Point out each Plasmodium parasite.
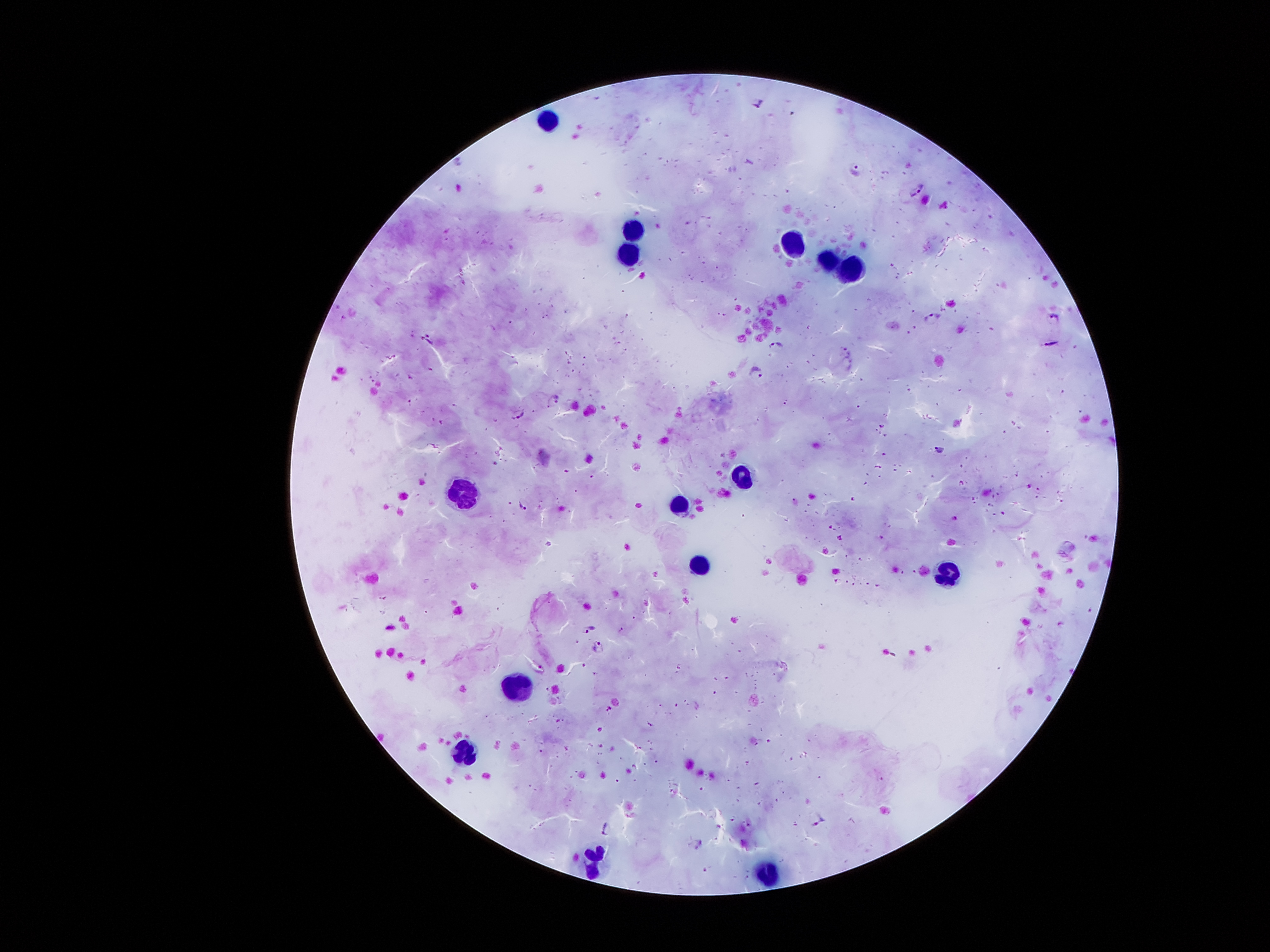
Approximate centers as [x, y] in pixels.
Plasmodium parasites: [758, 100], [857, 167], [917, 190], [933, 317], [1055, 318], [427, 338], [776, 342], [1052, 343], [844, 348], [850, 364], [755, 374], [552, 399], [517, 414], [939, 448], [522, 506], [587, 628], [598, 647], [538, 667], [817, 822], [605, 827], [698, 843].

leukocyte locations = [543, 119], [629, 230], [790, 240], [631, 257], [828, 260], [852, 271], [742, 474], [464, 490], [676, 500], [699, 564], [949, 573], [516, 682], [465, 755], [595, 861], [768, 868]
magnification = 100x
image size = 1270×952 pixels
preparation = thick blood smear
capture = smartphone through the microscope eyepiece
field of view = single
stain = Giemsa
patient malaria status = positive for Plasmodium falciparum